Assess this cell for malaria.
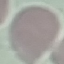

Uninfected.

Thin blood smear. Giemsa stain. Automatically extracted cell patch, resized to 64 × 64 pixels. Photographed with a smartphone camera at the microscope eyepiece.